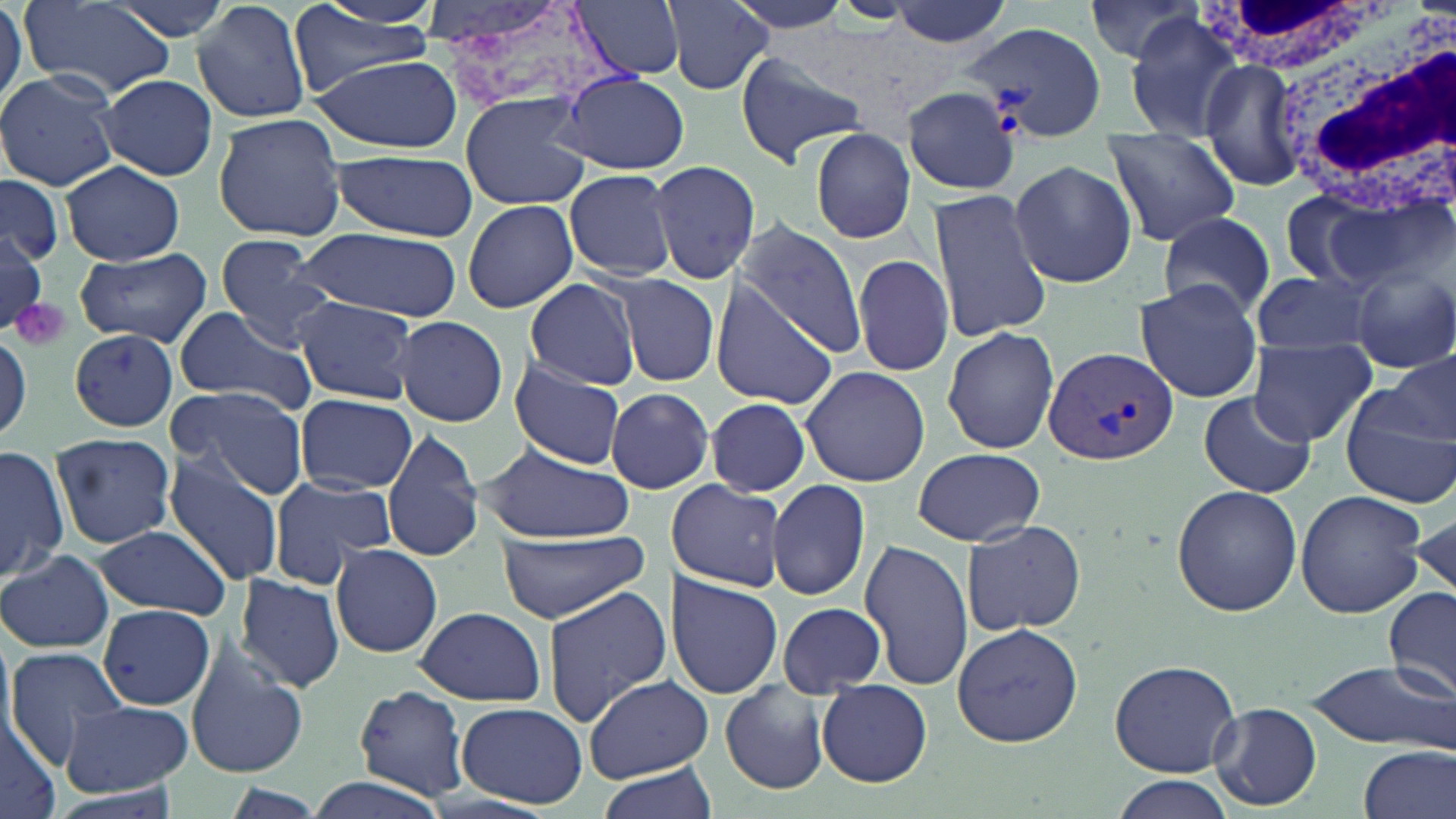
Summary:
  - Coordinate format: approximate bounding boxes as named x1/y1/x2/y2 corners in pixels
  - Plasmodium vivax-infected red blood cell locations: (x1=968, y1=22, x2=1104, y2=139), (x1=1042, y1=346, x2=1178, y2=465)
  - Uninfected red blood cell locations: (x1=105, y1=0, x2=237, y2=43), (x1=192, y1=0, x2=312, y2=124), (x1=305, y1=0, x2=445, y2=33), (x1=425, y1=0, x2=617, y2=118), (x1=571, y1=0, x2=687, y2=80), (x1=719, y1=0, x2=857, y2=39), (x1=23, y1=1, x2=174, y2=99), (x1=665, y1=1, x2=772, y2=95), (x1=882, y1=1, x2=1019, y2=47), (x1=1084, y1=1, x2=1201, y2=65), (x1=0, y1=2, x2=25, y2=107), (x1=288, y1=9, x2=438, y2=93), (x1=1120, y1=13, x2=1248, y2=140), (x1=734, y1=51, x2=868, y2=166), (x1=312, y1=53, x2=463, y2=153), (x1=1197, y1=60, x2=1304, y2=192), (x1=0, y1=69, x2=123, y2=191), (x1=559, y1=71, x2=690, y2=174), (x1=96, y1=74, x2=218, y2=182), (x1=904, y1=87, x2=1022, y2=196), (x1=460, y1=95, x2=590, y2=210), (x1=213, y1=111, x2=348, y2=242), (x1=807, y1=127, x2=916, y2=245), (x1=1101, y1=128, x2=1242, y2=246), (x1=329, y1=152, x2=478, y2=240), (x1=1008, y1=159, x2=1137, y2=288), (x1=60, y1=161, x2=184, y2=265), (x1=646, y1=161, x2=761, y2=284), (x1=563, y1=169, x2=678, y2=280), (x1=0, y1=174, x2=64, y2=265), (x1=927, y1=185, x2=1053, y2=343), (x1=462, y1=198, x2=579, y2=313), (x1=1155, y1=212, x2=1278, y2=323), (x1=733, y1=220, x2=869, y2=358), (x1=295, y1=227, x2=462, y2=319), (x1=0, y1=231, x2=49, y2=330), (x1=215, y1=235, x2=339, y2=347), (x1=73, y1=247, x2=213, y2=346), (x1=852, y1=253, x2=953, y2=380), (x1=1350, y1=260, x2=1456, y2=375), (x1=1251, y1=268, x2=1378, y2=359), (x1=615, y1=273, x2=720, y2=386), (x1=522, y1=279, x2=640, y2=389), (x1=711, y1=280, x2=839, y2=408), (x1=1135, y1=282, x2=1264, y2=405), (x1=295, y1=297, x2=420, y2=405), (x1=172, y1=306, x2=319, y2=415), (x1=395, y1=316, x2=509, y2=426), (x1=942, y1=324, x2=1060, y2=455), (x1=70, y1=329, x2=180, y2=430), (x1=0, y1=331, x2=31, y2=444), (x1=1248, y1=338, x2=1377, y2=446), (x1=1388, y1=353, x2=1456, y2=444), (x1=509, y1=360, x2=627, y2=468), (x1=800, y1=364, x2=929, y2=487), (x1=167, y1=384, x2=309, y2=499), (x1=606, y1=387, x2=715, y2=494), (x1=1339, y1=389, x2=1455, y2=510), (x1=1198, y1=392, x2=1317, y2=498), (x1=295, y1=393, x2=417, y2=494), (x1=701, y1=398, x2=812, y2=496), (x1=383, y1=426, x2=483, y2=564), (x1=49, y1=432, x2=177, y2=550), (x1=477, y1=442, x2=634, y2=542), (x1=0, y1=445, x2=69, y2=581), (x1=912, y1=446, x2=1045, y2=545), (x1=162, y1=452, x2=287, y2=586), (x1=267, y1=476, x2=396, y2=585), (x1=669, y1=478, x2=787, y2=593), (x1=768, y1=479, x2=871, y2=602), (x1=1170, y1=484, x2=1302, y2=617), (x1=1295, y1=491, x2=1427, y2=617), (x1=1410, y1=506, x2=1455, y2=605), (x1=962, y1=518, x2=1087, y2=636), (x1=94, y1=526, x2=233, y2=618), (x1=494, y1=532, x2=650, y2=622), (x1=860, y1=540, x2=975, y2=692), (x1=330, y1=543, x2=444, y2=658), (x1=1, y1=549, x2=114, y2=655), (x1=236, y1=576, x2=345, y2=691), (x1=668, y1=576, x2=782, y2=697), (x1=543, y1=585, x2=670, y2=724), (x1=1384, y1=587, x2=1456, y2=701), (x1=776, y1=602, x2=886, y2=697), (x1=99, y1=605, x2=217, y2=710), (x1=413, y1=605, x2=547, y2=707), (x1=951, y1=621, x2=1085, y2=749), (x1=185, y1=642, x2=308, y2=779), (x1=5, y1=648, x2=131, y2=768), (x1=1108, y1=657, x2=1242, y2=778), (x1=1305, y1=660, x2=1454, y2=752), (x1=586, y1=674, x2=712, y2=780), (x1=817, y1=680, x2=930, y2=786), (x1=719, y1=681, x2=830, y2=794), (x1=353, y1=685, x2=473, y2=800), (x1=62, y1=700, x2=191, y2=793), (x1=456, y1=702, x2=587, y2=808), (x1=1209, y1=703, x2=1321, y2=810), (x1=0, y1=713, x2=64, y2=819), (x1=1357, y1=746, x2=1455, y2=819), (x1=594, y1=762, x2=723, y2=819), (x1=299, y1=775, x2=453, y2=819), (x1=1110, y1=776, x2=1237, y2=819)
  - Platelet locations: (x1=11, y1=298, x2=70, y2=351)
  - White blood cell locations: (x1=1194, y1=0, x2=1416, y2=75), (x1=1273, y1=12, x2=1456, y2=219)
  - Slide-level diagnosis: Plasmodium vivax
  - Preparation: thin blood film
  - Image size: 1456×819 pixels
  - Modality: light microscopy
  - Magnification: 1000x
  - Stain: May-Grünwald-Giemsa
  - Field of view: one of a larger specimen